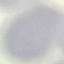

Malaria status: uninfected. Thin blood film. Giemsa-stained preparation. Photographed with a smartphone camera at the microscope eyepiece. Automatically extracted cell patch, resized to 64 × 64 pixels.